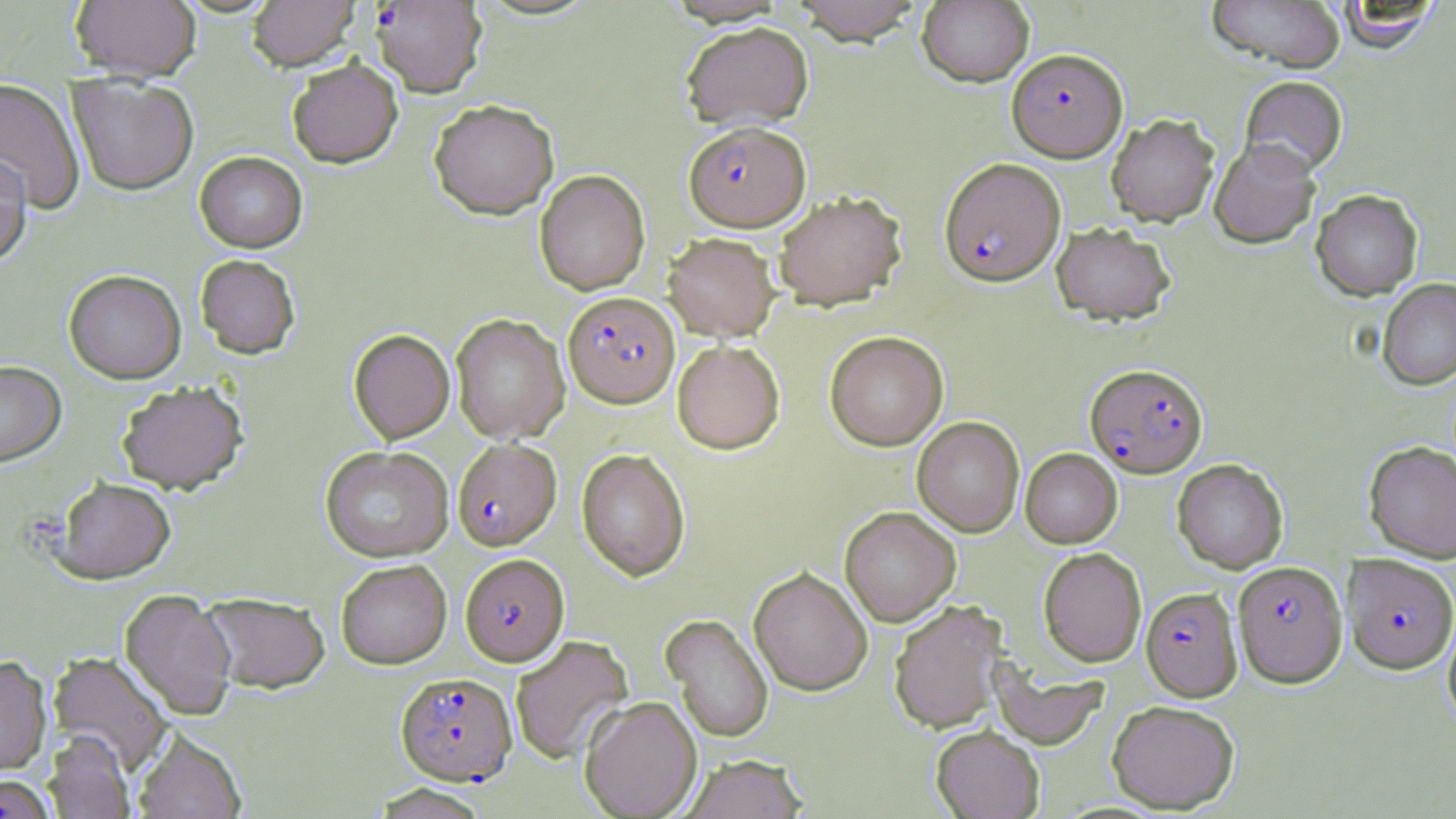

Summary:
  - Coordinate format: approximate bounding boxes as (x1, y1, x2, y2) in pixels
  - Platelet locations: (19, 509, 68, 565)
  - Plasmodium falciparum-infected red blood cell locations (subset): (372, 1, 487, 98), (1007, 47, 1128, 163), (684, 121, 810, 231), (940, 157, 1066, 285), (563, 291, 679, 408), (1085, 363, 1208, 478), (453, 438, 562, 550), (460, 553, 568, 666), (1343, 554, 1456, 674), (1233, 560, 1347, 688), (1141, 586, 1242, 701), (396, 671, 517, 785)
  - Uninfected red blood cell locations (subset): (70, 0, 201, 82), (248, 0, 359, 70), (790, 0, 925, 45), (917, 0, 1035, 87), (1208, 0, 1346, 73), (1332, 1, 1443, 53), (680, 21, 814, 131), (287, 57, 403, 168), (68, 75, 199, 195), (1240, 76, 1348, 176), (0, 78, 86, 213), (429, 99, 559, 219), (1106, 113, 1220, 226), (1209, 138, 1321, 249), (195, 151, 308, 252), (0, 152, 32, 268), (535, 169, 650, 295), (1311, 189, 1423, 300), (772, 190, 907, 310), (1052, 222, 1176, 325), (663, 232, 779, 341), (195, 254, 301, 358), (64, 269, 187, 383), (1377, 278, 1456, 390), (451, 313, 569, 443), (349, 329, 455, 443), (825, 331, 949, 451), (672, 340, 785, 454), (0, 360, 66, 466), (116, 380, 249, 494), (912, 416, 1024, 537), (1364, 441, 1456, 563), (320, 445, 453, 561), (576, 448, 690, 581), (1020, 448, 1122, 547), (1172, 459, 1288, 573), (51, 476, 176, 584), (840, 506, 961, 626), (1038, 547, 1147, 666), (336, 559, 451, 669), (749, 566, 873, 695), (119, 588, 237, 721), (201, 592, 331, 694), (888, 599, 1008, 733), (1443, 611, 1456, 729), (661, 614, 774, 743), (511, 635, 634, 765), (48, 652, 174, 775), (0, 655, 52, 775), (991, 664, 1108, 749), (580, 695, 702, 818), (1107, 700, 1240, 813), (931, 725, 1044, 819), (133, 728, 247, 818), (44, 731, 134, 819), (680, 754, 807, 819)
  - Slide-level diagnosis: Plasmodium falciparum
  - Modality: light microscopy
  - Image size: 1456×819 pixels
  - Stain: May-Grünwald-Giemsa
  - Magnification: 1000x
  - Preparation: thin blood smear
  - Field of view: single